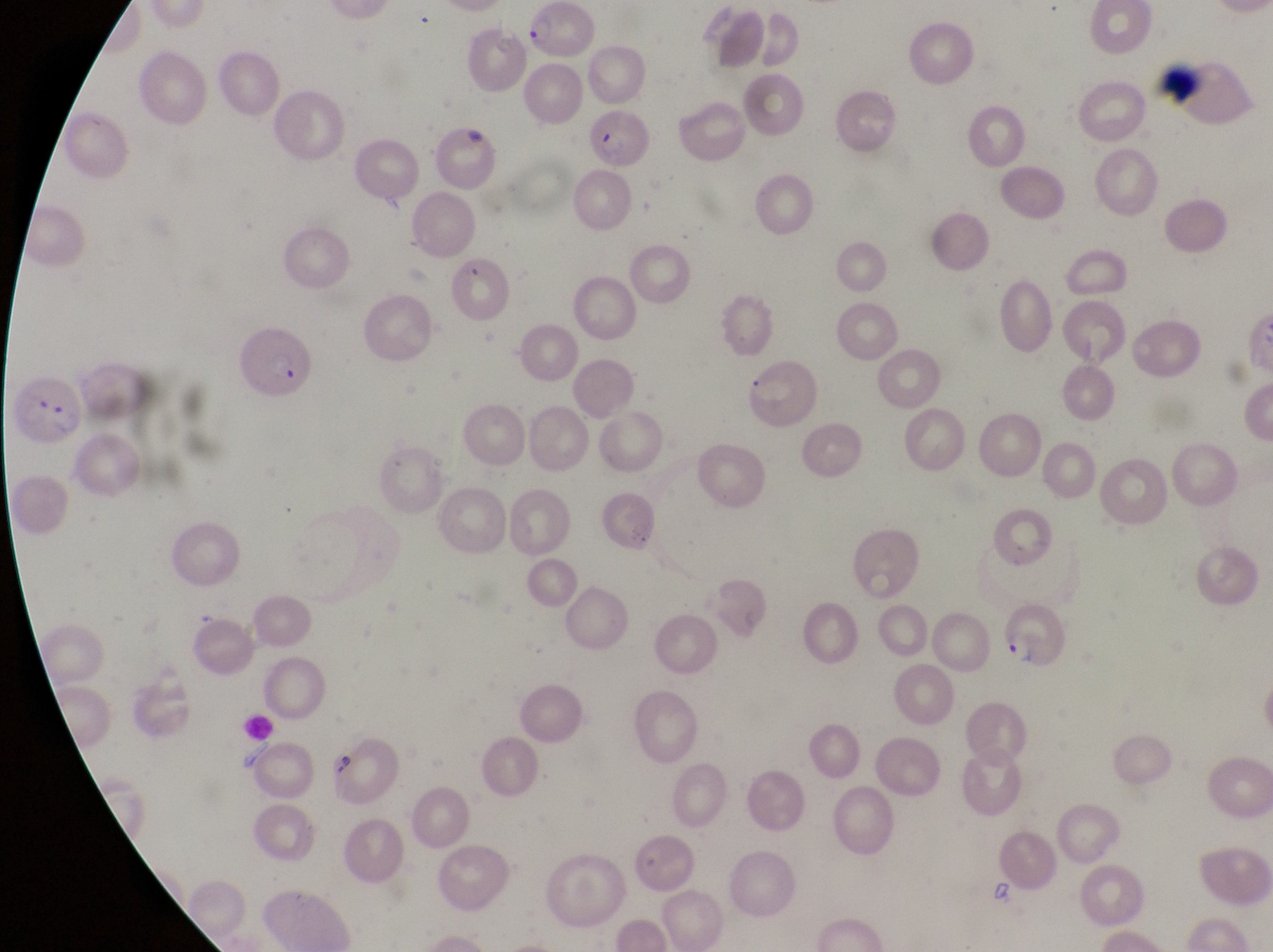 Approximate bounding boxes as (left, top, right, bottom) in pixels. Parasitised red blood cell locations: (530, 3, 600, 60), (1155, 61, 1205, 107), (587, 100, 649, 170), (230, 327, 315, 401), (13, 382, 87, 452), (996, 599, 1066, 669), (324, 725, 399, 799). Single field of view. Captured by a smartphone held over the eyepiece of an Olympus CX-23 microscope. Image is 1273×952 pixels. Sample from Uganda. At a magnification of 1000x. Thin blood film.